State the preparation type.
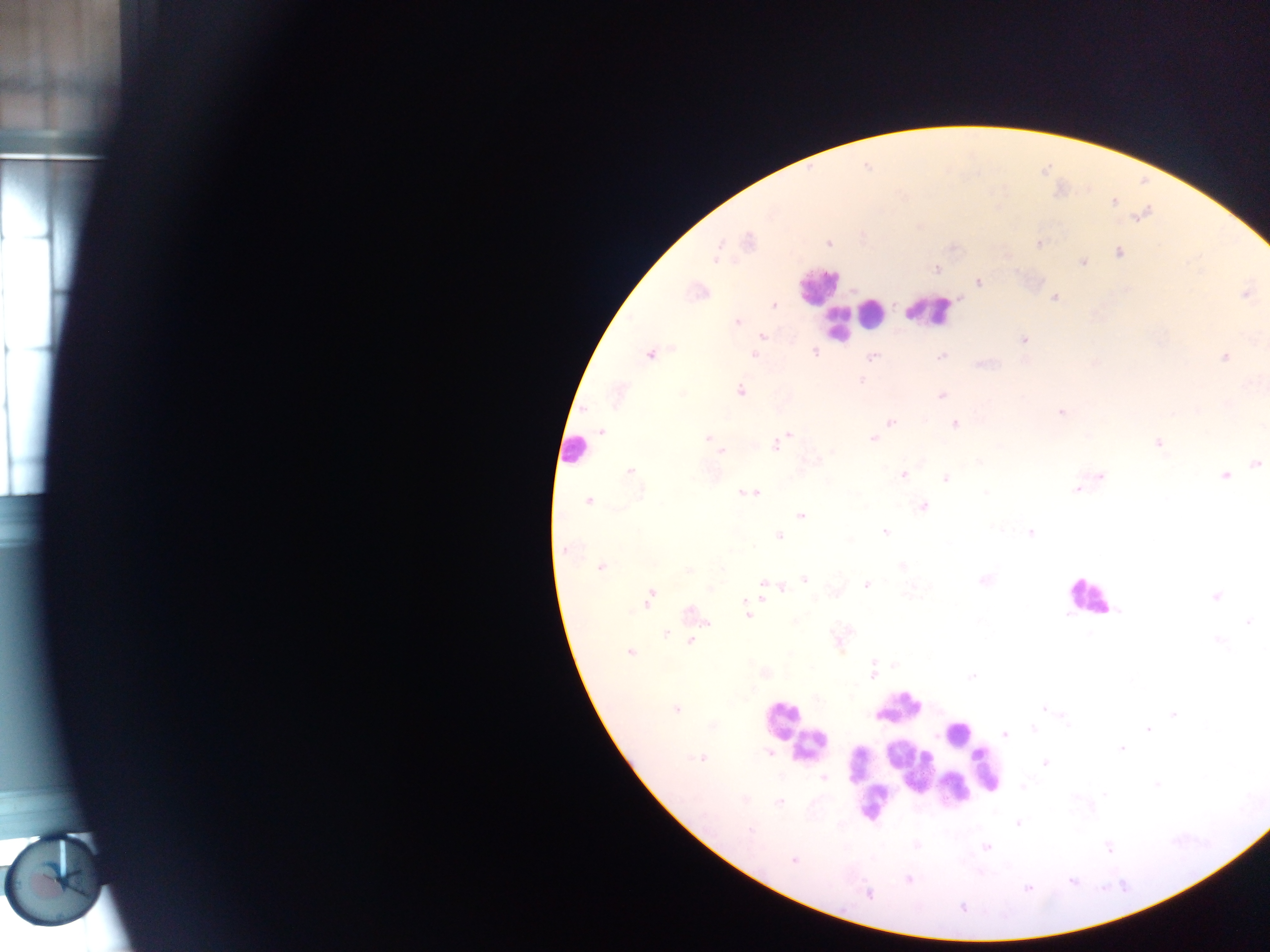
This is a thick smear.

Approximate centers as [x, y] in pixels. Leukocyte locations: [817, 286], [848, 310], [928, 311], [869, 312], [838, 323], [571, 450], [1089, 596], [898, 706], [781, 718], [957, 733], [809, 745], [901, 754], [911, 763], [857, 764], [986, 769], [937, 773], [953, 788], [874, 800]. Malaria parasite locations: [748, 241], [829, 242], [1039, 243], [1118, 252], [715, 257], [1082, 262], [937, 268], [978, 282], [696, 290], [1247, 292], [1053, 297], [772, 304], [736, 322], [762, 336], [1024, 339], [814, 352], [650, 353], [755, 354], [871, 357], [941, 357], [1224, 357], [739, 390], [942, 395], [1061, 412], [890, 421], [955, 424], [601, 432], [789, 434], [873, 438], [709, 439], [1158, 442], [775, 445], [721, 450], [1255, 463], [629, 471], [903, 474], [1226, 475], [1099, 476], [946, 478], [1078, 489], [750, 493], [588, 501], [923, 506], [801, 515], [886, 531], [1030, 532], [779, 535], [565, 549], [599, 566], [901, 566], [805, 579], [983, 580], [763, 583], [866, 584], [783, 589], [1216, 596], [648, 598], [691, 614], [747, 614], [1247, 622], [692, 636], [692, 640], [838, 640], [1217, 640], [630, 653], [873, 670], [764, 673], [675, 708], [1043, 709], [1034, 727], [1148, 728], [1004, 733], [1121, 749], [700, 757], [1045, 763], [823, 779], [779, 801], [1018, 822], [915, 845], [987, 846], [793, 860], [908, 879], [1027, 887], [868, 894]. Single field of view. Sample from Ghana. Photographed through a microscope with a mobile-phone camera. Image is 1270×952 pixels.